Evaluate for Plasmodium parasites.
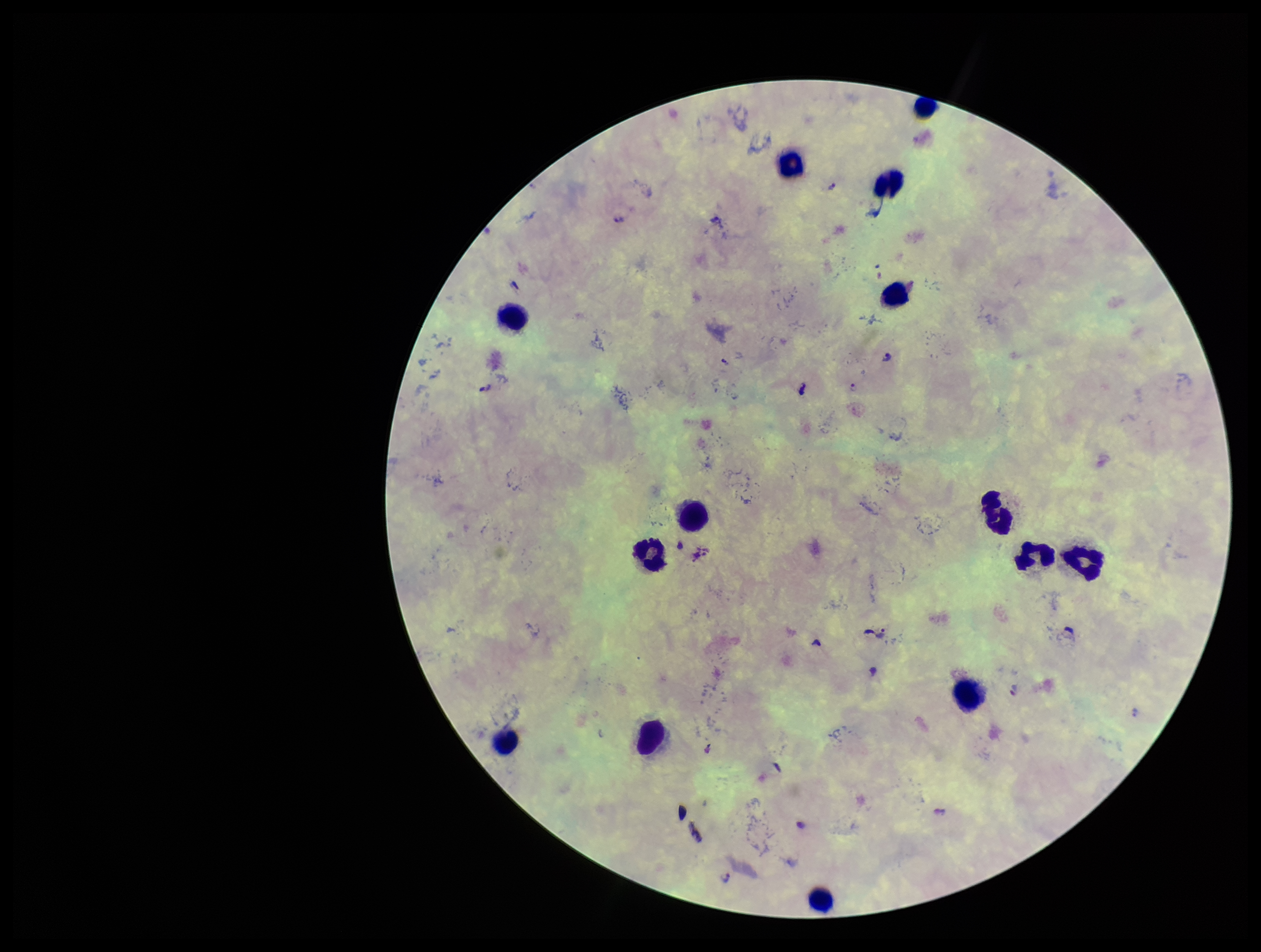

Identified.

Species reported for this patient: Plasmodium falciparum. Stained with Giemsa. Single field of view. Preparation: thick. Smartphone photograph taken through the eyepiece of a microscope. Patient malaria status: positive. Parasite count: 7. Leukocyte count: 14. Image is 1261×952 pixels.